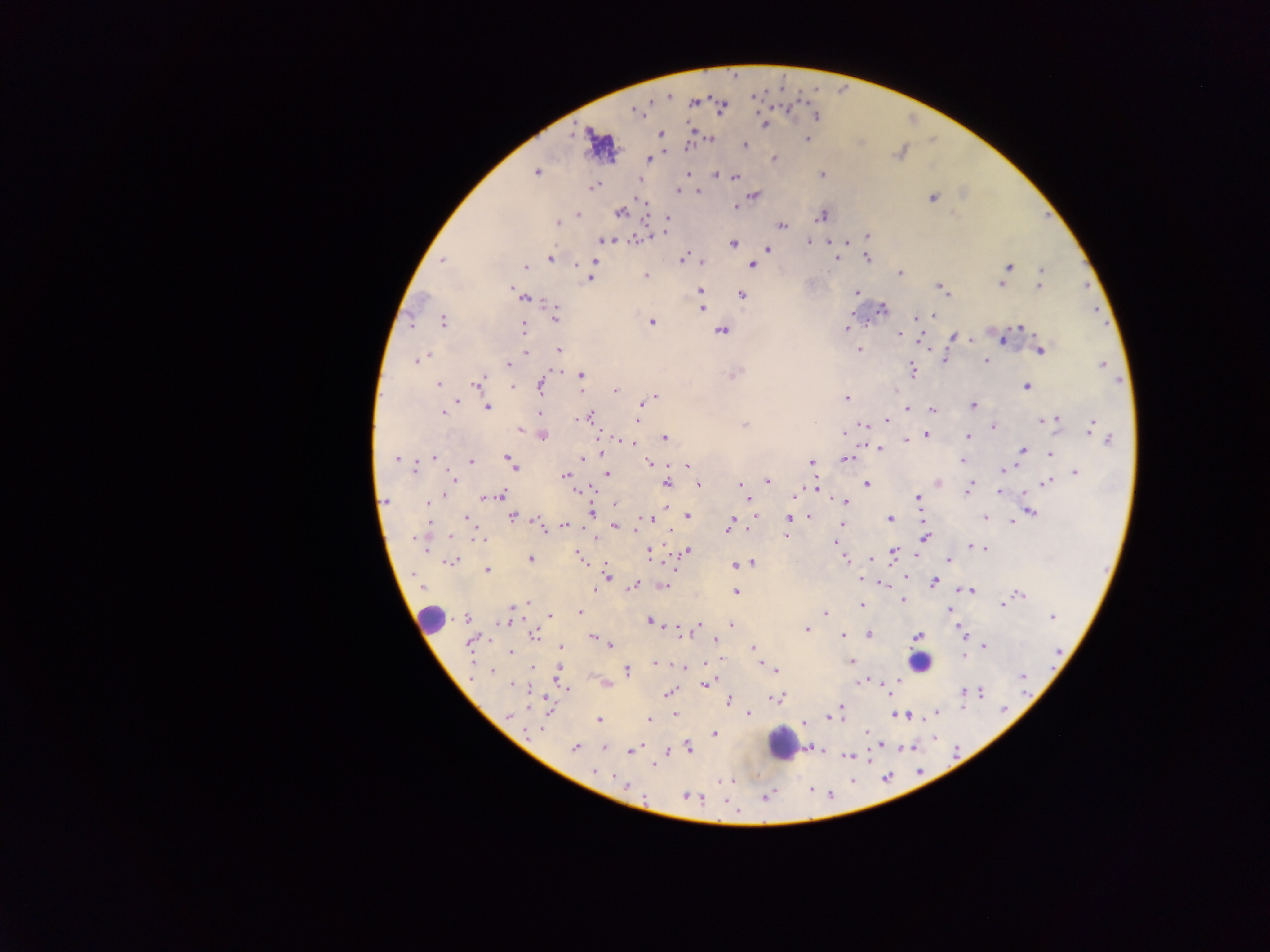
Approximate centers as x y in pixels. Malaria parasite locations (subset; some below the resolvable size): 669 96; 694 103; 635 110; 816 116; 764 125; 661 135; 711 139; 807 139; 689 145; 745 145; 900 152; 773 158; 649 160; 536 173; 687 174; 822 174; 717 175; 734 177; 640 179; 593 187; 677 191; 698 191; 754 196; 932 197; 640 200; 737 206; 620 213; 579 215; 1049 215; 822 216; 667 217; 557 223; 782 226; 665 232; 868 236; 637 239; 606 240; 808 242; 831 242; 846 242; 733 243; 768 249; 867 257; 549 258; 682 259; 838 259; 442 261; 594 262; 702 262; 751 264; 526 267; 1009 267; 1042 271; 900 273; 645 276; 590 279; 1085 284; 1001 285; 1039 286; 940 288; 701 289; 511 290; 856 292; 742 295; 525 298; 702 309; 883 309; 932 315; 556 316; 915 318; 443 322; 653 322; 1105 322; 1021 327; 523 329; 846 329; 722 331; 898 334; 954 336; 971 339; 1003 339; 859 349; 559 350; 1040 351; 526 352; 426 356; 945 360; 418 361; 986 361; 508 364; 1102 364; 912 369; 735 374; 581 375; 476 383; 438 384; 540 385; 1026 386; 512 387; 614 391; 655 396; 847 398; 641 405; 487 406; 972 406; 907 409; 934 410; 443 413; 540 414; 591 415; 583 417; 636 420; 1054 420; 887 421; 1045 421; 864 424; 745 426; 1092 426; 994 428; 519 430; 844 433; 927 434; 543 435; 664 437; 967 437; 907 440; 1109 440; 630 444; 879 449; 1022 450; 1051 453; 601 454; 434 457; 506 458; 582 458; 396 459; 846 459; 963 460; 470 462; 649 462; 811 462; 511 463; 686 466; 415 467; 1004 469; 1076 473; 607 474; 565 475; 451 478; 768 481; 1048 482; 938 483; 666 484; 866 484; 699 485; 740 485; 589 489; 815 489; 968 489; 578 491; 1000 492; 444 495; 501 495; 491 496; 917 496; 484 497; 748 499; 386 500; 429 502; 846 502; 614 504; 590 513; 1031 513; 466 516; 687 516; 809 516; 512 517; 986 517; 652 519; 789 519; 890 519; 430 521; 536 521; 732 522; 1012 522; 565 525; 841 525; 615 526; 541 527; 729 527; 451 537; 786 537; 925 539; 418 540; 478 540; 837 541; 972 546; 984 548; 687 551; 649 553; 893 554; 578 556; 531 559; 844 559; 871 560; 949 560; 450 562; 752 563; 734 566; 486 570; 606 575; 933 582; 882 584; 633 586; 594 589; 969 589; 736 591; 1020 595; 903 600; 528 602; 861 605; 1002 605; 517 606; 949 609; 826 612; 580 613; 550 616; 1052 617; 467 619; 504 621; 651 621; 731 624; 700 625; 807 629; 680 632; 961 632; 535 635; 869 635; 842 636; 918 636; 592 637; 715 640; 471 642; 610 645; 984 646; 561 647; 753 648; 1057 650; 511 652; 964 656; 852 662; 656 664; 685 668; 533 669; 775 670; 627 671; 492 672; 1023 676; 860 682; 607 684; 512 685; 705 685; 567 688; 887 689; 668 692; 966 692; 980 692; 775 699; 729 701; 840 708; 936 712; 749 713; 675 714; 835 715; 905 715; 509 716; 599 720; 648 720; 867 732; 715 734; 878 745; 953 745; 689 747; 574 748; 604 748; 900 748; 631 750; 847 756; 928 763; 654 765; 594 771; 731 781; 625 785; 815 787; 769 796; 688 797. Leukocyte locations: 431 617; 921 662; 785 744. Collected in Ghana. Photographed through a microscope with a mobile-phone camera. Image is 1270×952 pixels. Thick blood smear. Single field of view.